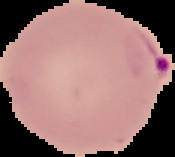
image_type: segmented cell region on a black background
result: malaria parasites identified
image_size: 175×157 pixels
preparation: thin blood smear